Assess this cell for malaria.
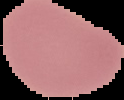
Uninfected.

image type = cell region segmented out of the field of view; surrounding area masked to black
preparation = thin blood film
image size = 124×100 pixels